State which parasite is depicted.
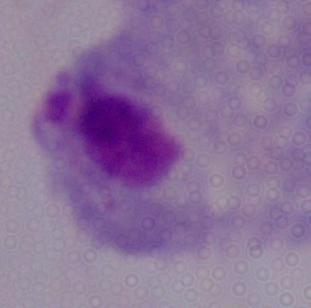

This is a trichomonad.

Photomicrograph. Captured at 1000x magnification.